Classify this cell by malaria status.
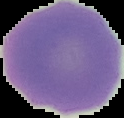

It is uninfected.

Image is 124×118 pixels. The area outside the segmented cell region is set to black. From a thin blood film.